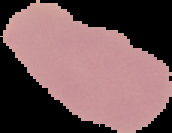
image type = segmented cell region with the area outside set to black
result = no malaria parasites seen
preparation = thin blood smear
image size = 172×133 pixels